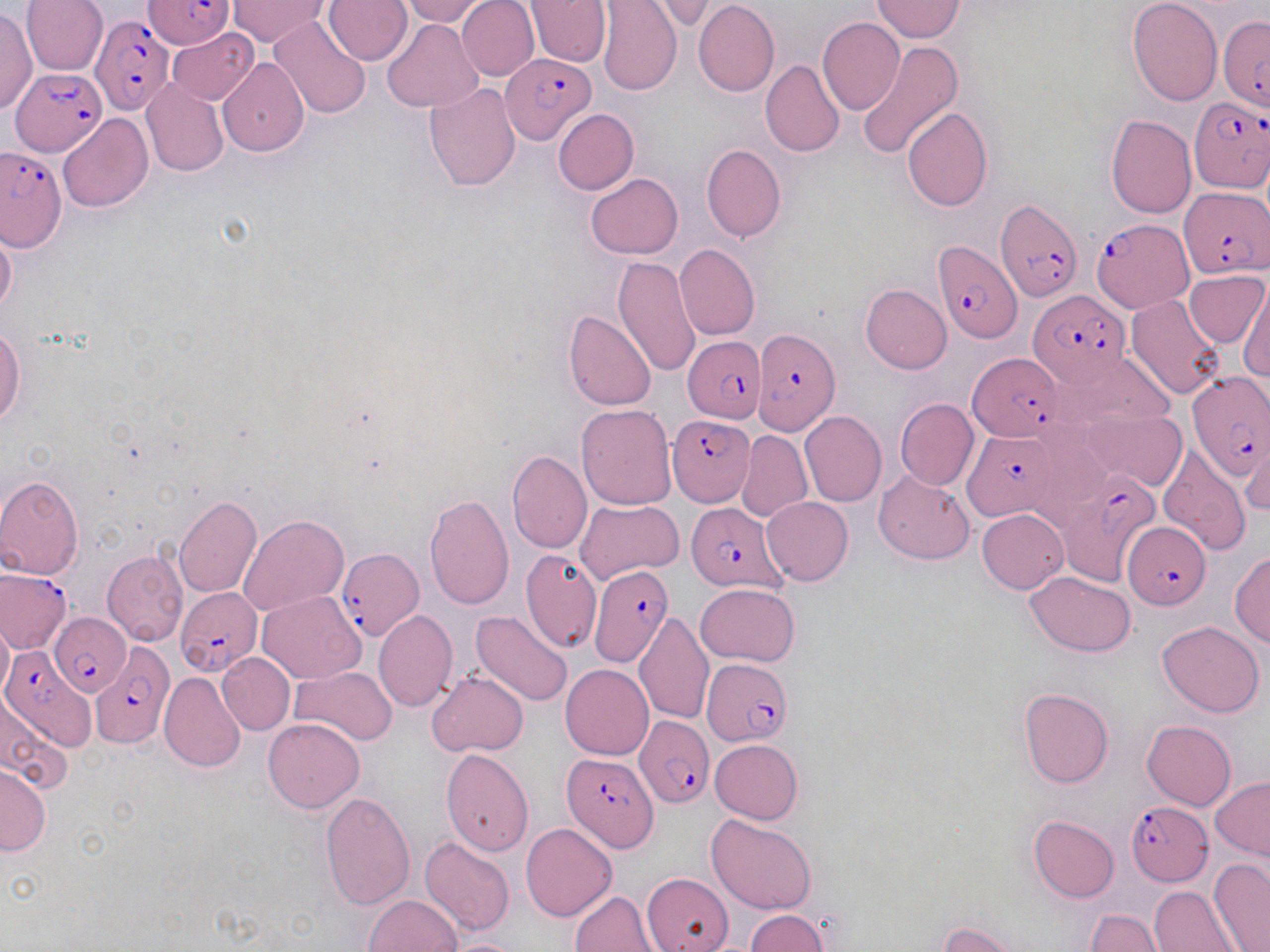

Approximate bounding boxes as (x1, y1, x2, y2) in pixels. Uninfected red blood cell locations: (22, 0, 108, 75), (400, 0, 487, 25), (456, 0, 539, 82), (524, 0, 611, 67), (596, 0, 682, 96), (1128, 0, 1223, 105), (228, 1, 329, 48), (324, 1, 411, 65), (692, 1, 778, 97), (872, 1, 964, 42), (0, 8, 36, 114), (267, 15, 371, 120), (818, 17, 905, 117), (382, 20, 483, 113), (168, 27, 260, 105), (856, 40, 966, 161), (218, 59, 309, 156), (761, 59, 844, 157), (141, 78, 228, 177), (423, 81, 521, 191), (902, 107, 992, 212), (553, 108, 638, 194), (57, 113, 152, 213), (1105, 114, 1197, 219), (701, 143, 786, 242), (586, 173, 682, 259), (0, 223, 17, 318), (675, 243, 760, 340), (613, 256, 701, 379), (1185, 270, 1267, 347), (1143, 279, 1264, 373), (861, 284, 952, 374), (1239, 286, 1269, 382), (1125, 294, 1226, 401), (564, 310, 656, 410), (0, 326, 26, 426), (895, 398, 979, 491), (577, 403, 678, 509), (1083, 409, 1186, 490), (799, 411, 887, 507), (738, 430, 812, 523), (1240, 442, 1270, 517), (1157, 443, 1249, 555), (507, 448, 591, 554), (874, 469, 974, 564), (0, 473, 83, 579), (424, 493, 514, 608), (173, 495, 262, 597), (762, 496, 854, 585), (575, 500, 683, 584), (977, 508, 1068, 593), (238, 515, 348, 617), (517, 548, 600, 651), (102, 551, 190, 647), (1230, 551, 1270, 646), (1025, 571, 1136, 656), (695, 584, 802, 666), (256, 590, 366, 684), (374, 611, 458, 712), (471, 611, 574, 707), (634, 612, 714, 726), (0, 617, 13, 700), (1157, 621, 1265, 718), (217, 652, 295, 735), (561, 663, 653, 759), (288, 665, 397, 746), (427, 670, 527, 756), (159, 672, 245, 773), (1017, 687, 1114, 789), (0, 690, 74, 794), (263, 717, 365, 813), (1142, 720, 1236, 810), (710, 739, 803, 824), (440, 747, 534, 856), (0, 764, 50, 855), (1210, 776, 1270, 860), (320, 792, 416, 910), (706, 814, 818, 915), (1029, 815, 1119, 902), (520, 822, 617, 921), (420, 836, 514, 938), (1208, 858, 1270, 952), (641, 873, 733, 952), (1150, 886, 1240, 952), (570, 890, 660, 951), (362, 894, 462, 952), (744, 909, 829, 951), (1085, 910, 1167, 952), (939, 921, 1025, 951), (445, 939, 524, 952). Plasmodium falciparum-infected red blood cell locations: (145, 0, 233, 51), (142, 1, 233, 50), (91, 14, 175, 114), (1218, 16, 1270, 112), (501, 53, 595, 144), (10, 68, 105, 155), (1187, 95, 1270, 194), (1, 147, 67, 250), (1181, 185, 1268, 278), (997, 198, 1082, 301), (1091, 217, 1193, 313), (932, 241, 1020, 344), (1027, 291, 1134, 391), (753, 327, 841, 435), (684, 335, 765, 422), (967, 353, 1068, 442), (1186, 372, 1269, 479), (667, 416, 755, 506), (961, 429, 1061, 520), (1059, 470, 1163, 583), (685, 501, 785, 591), (1123, 520, 1209, 609), (335, 547, 426, 642), (587, 565, 674, 666), (1, 569, 71, 653), (176, 587, 261, 676), (48, 613, 131, 696), (92, 642, 175, 748), (1, 646, 85, 749), (702, 660, 792, 747), (634, 716, 715, 807), (561, 753, 657, 852), (1126, 802, 1213, 884). Slide-level diagnosis: Plasmodium falciparum. Light microscopy. Captured at 1000x magnification. Thin blood film. May-Grünwald-Giemsa stain. Image is 1270×952 pixels. One field of a larger specimen.